Locate every blood parasite and identify its species.
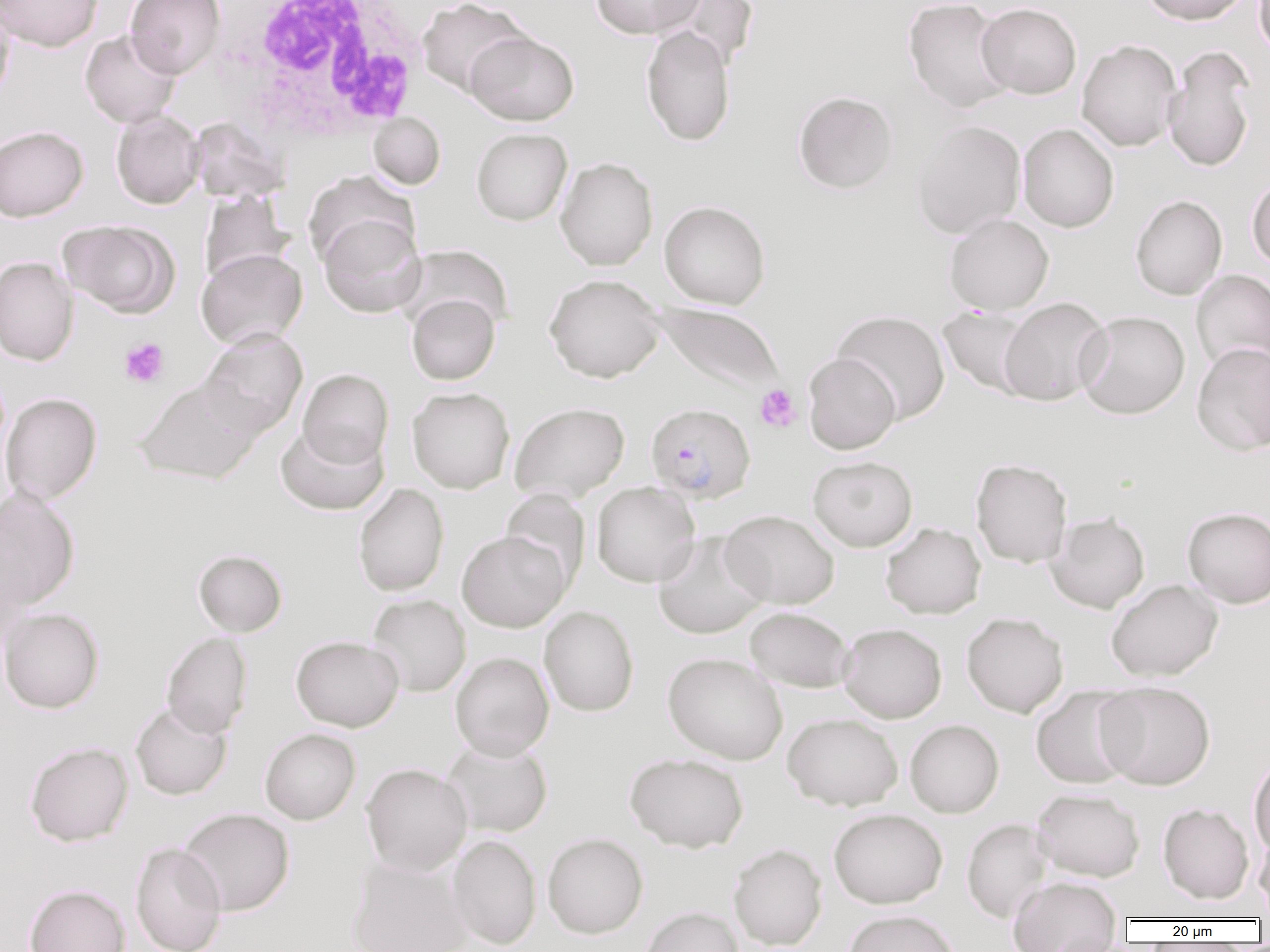

Approximate bounding boxes as (x1,y1)-(x2,y2) corner pairs in pixels.
Plasmodium falciparum-infected red blood cells: (646,403)-(756,503).
No Plasmodium ovale, Plasmodium malariae, Plasmodium vivax, Babesia divergens, or Trypanosoma brucei observed.

slide_level_diagnosis: Plasmodium falciparum
modality: light microscopy
image_size: 1270×952 pixels
uninfected_red_blood_cell_locations: 'approximate bounding boxes as (x1,y1)-(x2,y2) corner pairs in pixels: (1,0)-(103,51), (126,0)-(226,78), (416,0)-(531,97), (590,0)-(705,39), (660,0)-(759,70), (903,0)-(1014,113), (1137,0)-(1253,25), (1255,0)-(1270,60), (976,3)-(1082,99), (0,6)-(14,103), (641,26)-(736,146), (80,29)-(182,128), (466,31)-(579,125), (1076,39)-(1182,151), (1162,45)-(1257,172), (793,91)-(898,194), (111,110)-(204,209), (368,112)-(445,189), (187,118)-(291,203), (911,120)-(1025,238), (1018,124)-(1119,232), (0,125)-(88,221), (471,128)-(572,226), (555,157)-(658,271), (303,171)-(418,269), (1247,175)-(1270,271), (198,190)-(294,287), (1130,195)-(1227,300), (659,200)-(771,309), (318,213)-(427,318), (944,213)-(1054,315), (58,220)-(178,318), (397,245)-(513,336), (196,249)-(307,350), (0,256)-(79,366), (1191,269)-(1270,374), (544,274)-(665,383), (407,294)-(500,385), (998,297)-(1112,406), (646,300)-(785,396), (938,306)-(1038,399), (831,310)-(951,423), (1076,311)-(1190,419), (199,328)-(307,438), (1192,343)-(1270,456), (802,353)-(900,454), (297,368)-(394,468), (134,379)-(263,484), (407,387)-(514,494), (1,393)-(102,504), (509,402)-(629,502), (275,422)-(388,516), (808,455)-(918,551), (971,458)-(1073,567), (591,481)-(701,587), (353,483)-(449,596), (0,487)-(80,612), (501,489)-(590,590), (1182,507)-(1270,608), (720,509)-(839,609), (1045,511)-(1150,613), (880,522)-(986,619), (457,530)-(571,632), (653,532)-(768,639), (193,549)-(288,636), (1106,578)-(1223,681), (367,593)-(471,696), (539,605)-(639,717), (0,607)-(104,713), (745,607)-(855,692), (961,612)-(1068,717), (838,623)-(947,723), (161,632)-(253,739), (291,635)-(404,731), (450,651)-(554,760), (663,652)-(788,764), (1096,680)-(1216,790), (1030,686)-(1140,789), (130,702)-(232,800), (782,712)-(903,811), (904,719)-(1004,818), (260,728)-(361,825), (442,738)-(553,837), (25,742)-(133,846), (625,752)-(749,853), (1248,752)-(1270,860), (361,763)-(473,876), (1032,787)-(1145,882), (1158,803)-(1254,904), (177,807)-(295,916), (828,808)-(947,908), (962,818)-(1054,922), (542,832)-(648,938), (1254,832)-(1270,913), (448,834)-(541,950), (130,842)-(228,952), (728,843)-(827,950), (347,858)-(471,952), (1008,875)-(1122,950), (24,884)-(130,952), (639,906)-(744,952), (842,909)-(960,952)'
field_of_view: one of a larger specimen
preparation: thin blood film
magnification: 1000x
platelet_locations: 'approximate bounding boxes as (x1,y1)-(x2,y2) corner pairs in pixels: (119,338)-(170,388), (755,384)-(802,433)'
white_blood_cell_locations: 'approximate bounding boxes as (x1,y1)-(x2,y2) corner pairs in pixels: (219,1)-(432,144)'